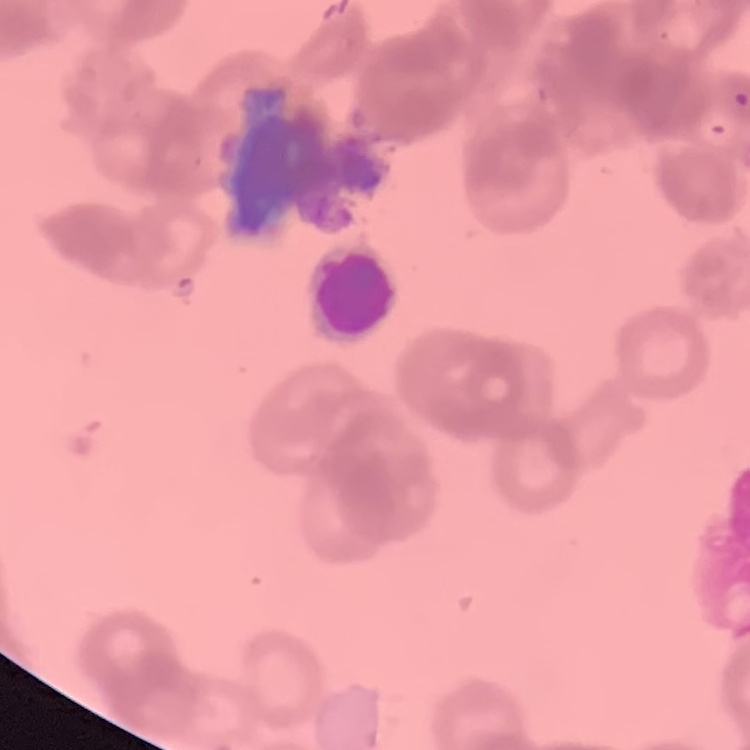 The red blood cells exhibit rouleaux formation. Thin blood smear. Stained with either Field's or Giemsa. Square crop of a larger photomicrograph.